Comment on the morphology of the red blood cells.
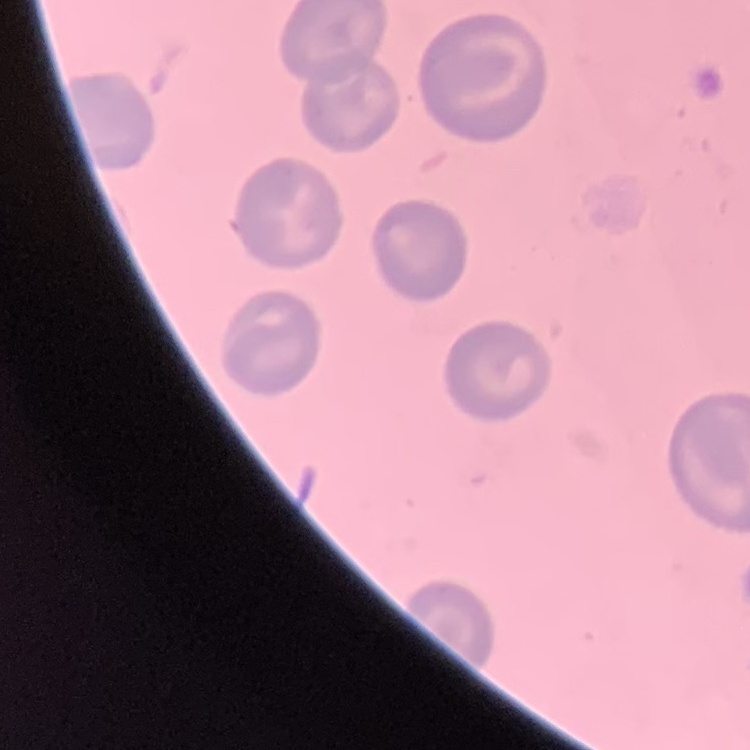
No rouleaux formation.

Summary:
  - Stain: Field's or Giemsa
  - Image type: one tile cut from a larger photomicrograph
  - Preparation: thin peripheral smear